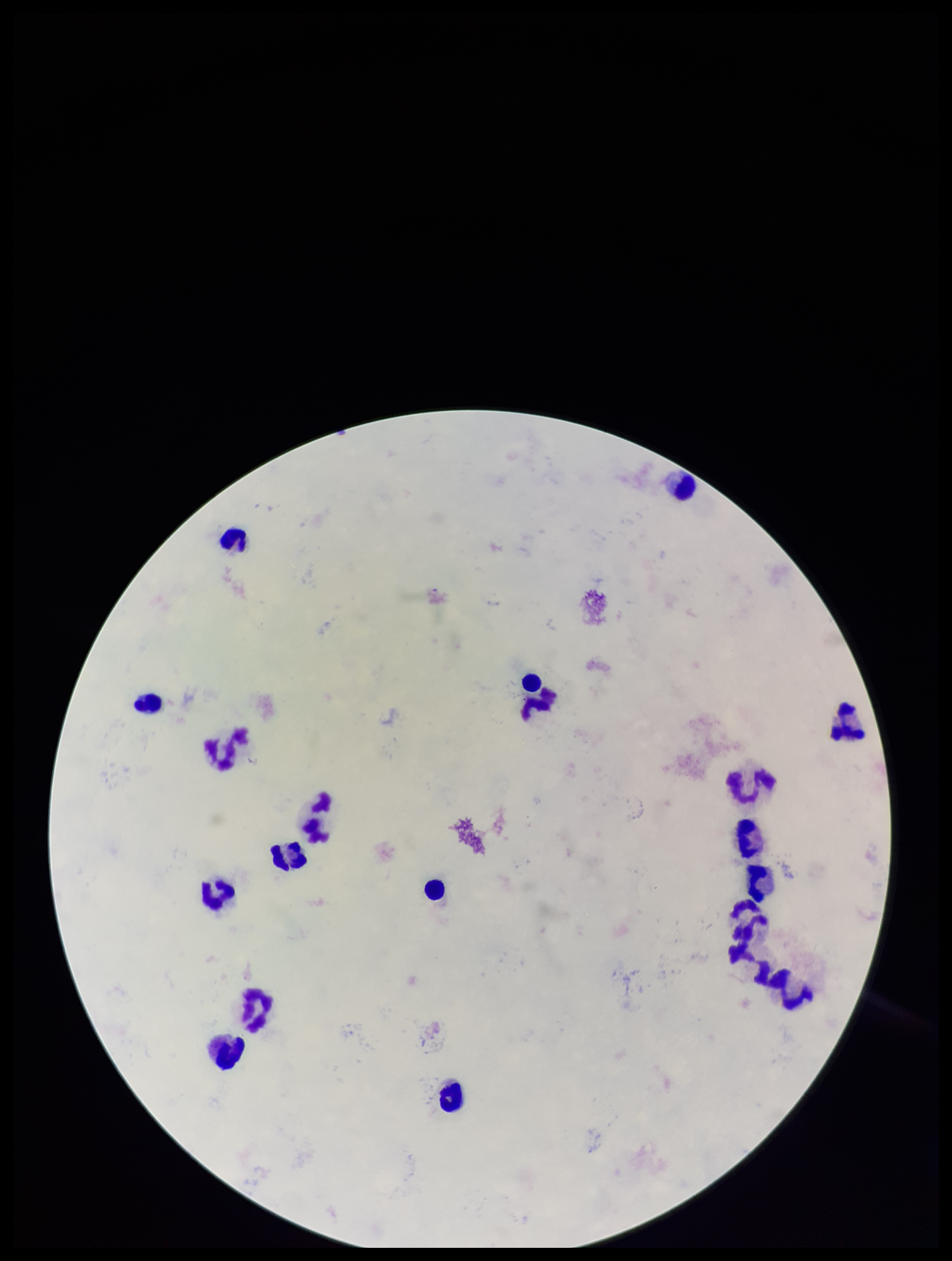
image size = 952×1261 pixels
field of view = one from this slide
patient malaria status = negative
preparation = thick blood smear
stain = Giemsa
capture = smartphone photograph through the microscope eyepiece
leukocyte count = 20
parasite count = 0
Plasmodium parasites = none detected